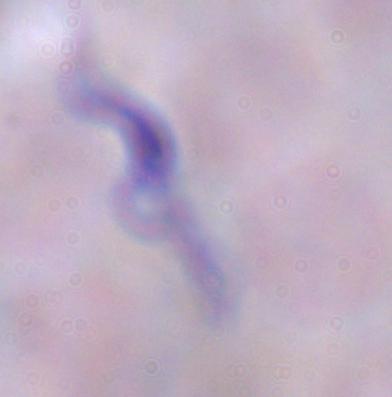
Micrograph. A trypanosome is seen. Captured at 1000x magnification.